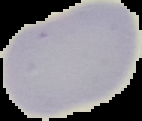
Summary:
  - Malaria status: uninfected
  - Image size: 142×121 pixels
  - Image type: segmented cell region with the area outside set to black
  - Preparation: thin blood smear